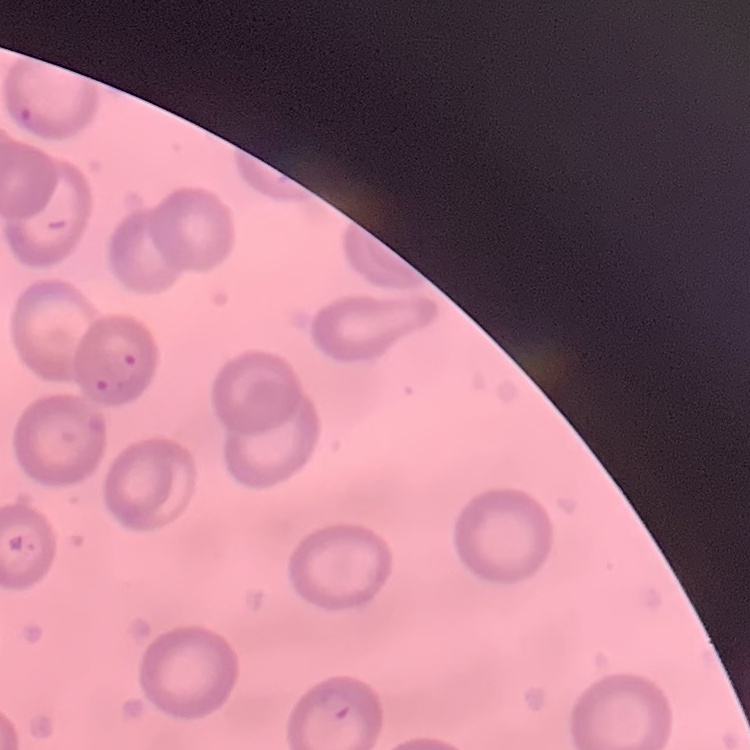

The erythrocytes exhibit no rouleaux formation. One tile cut from a larger photomicrograph. Thin peripheral smear. Field's or Giemsa stain.